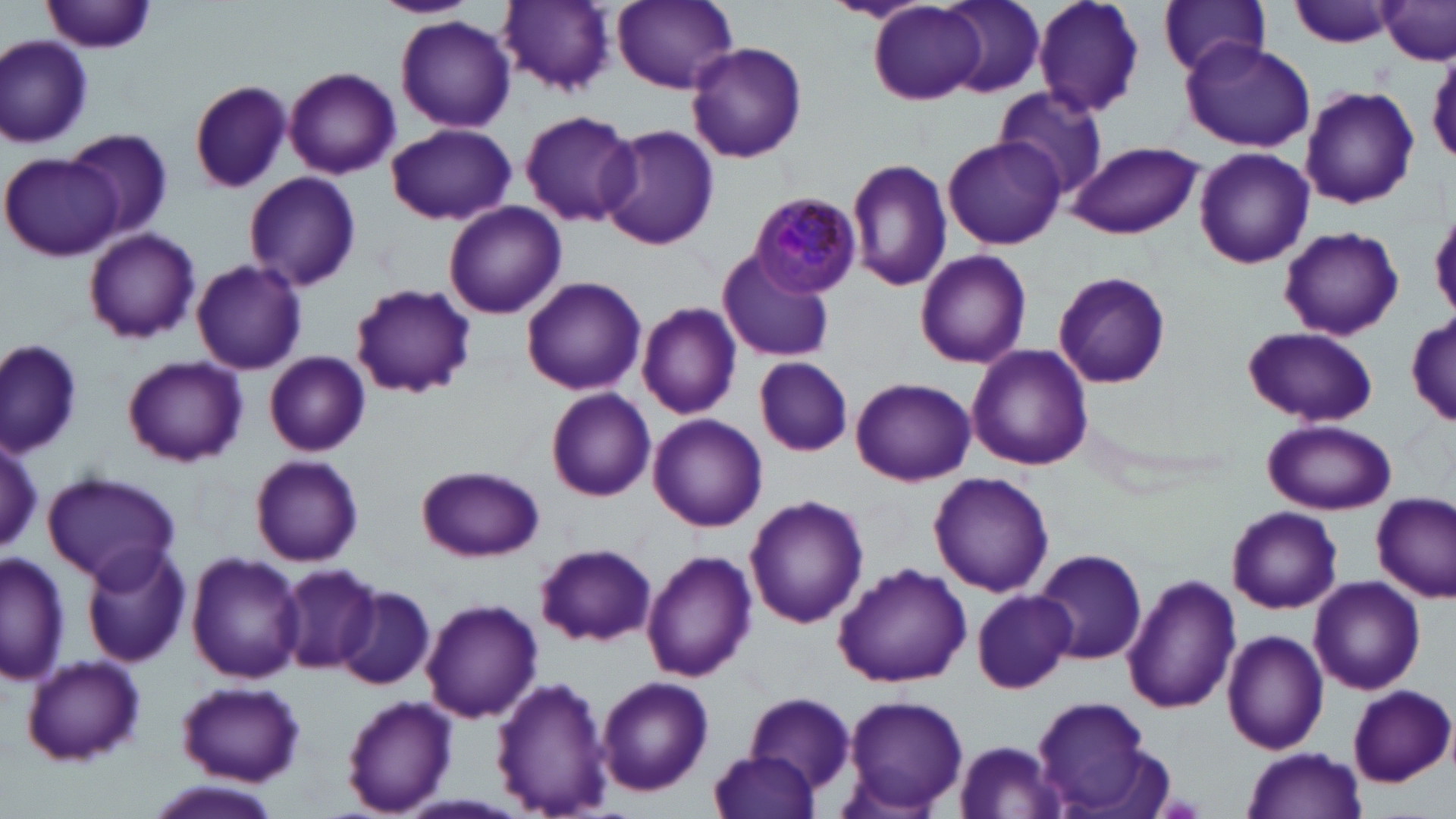

Approximate bounding boxes as [x1, y1, x2, y2] in pixels. Uninfected red blood cell locations: [374, 0, 476, 18], [497, 0, 615, 94], [612, 0, 739, 92], [824, 0, 933, 25], [941, 0, 1045, 97], [1031, 0, 1145, 120], [1158, 0, 1270, 78], [1287, 0, 1399, 49], [43, 1, 156, 55], [1379, 1, 1455, 64], [869, 2, 987, 104], [395, 15, 517, 133], [0, 34, 95, 148], [1179, 39, 1316, 152], [686, 41, 808, 165], [284, 66, 401, 179], [190, 80, 292, 193], [992, 85, 1108, 200], [1300, 86, 1420, 209], [519, 108, 639, 228], [387, 124, 515, 225], [597, 125, 720, 251], [67, 127, 172, 240], [943, 138, 1065, 250], [1066, 141, 1202, 240], [1193, 147, 1315, 269], [2, 151, 126, 259], [847, 158, 952, 292], [243, 170, 362, 291], [442, 200, 567, 320], [1278, 226, 1405, 342], [83, 227, 200, 343], [717, 247, 835, 362], [915, 249, 1033, 369], [191, 259, 306, 375], [1052, 270, 1171, 390], [520, 278, 647, 397], [350, 284, 477, 399], [637, 300, 743, 420], [1408, 314, 1455, 428], [1242, 326, 1381, 429], [1, 337, 85, 458], [966, 344, 1094, 471], [264, 352, 370, 456], [122, 355, 247, 466], [754, 357, 854, 456], [851, 377, 976, 487], [546, 389, 656, 504], [647, 413, 767, 531], [1264, 419, 1397, 514], [2, 430, 43, 558], [250, 455, 364, 566], [416, 464, 544, 562], [43, 470, 183, 587], [930, 470, 1055, 596], [1372, 493, 1455, 600], [745, 494, 869, 629], [1226, 505, 1343, 615], [79, 542, 192, 667], [535, 543, 658, 647], [1031, 546, 1149, 665], [642, 549, 757, 683], [2, 552, 69, 687], [187, 553, 303, 683], [832, 562, 973, 687], [275, 566, 379, 673], [1122, 574, 1241, 715], [1308, 575, 1428, 694], [335, 586, 434, 689], [971, 588, 1076, 692], [422, 597, 542, 722], [1223, 630, 1329, 755], [20, 654, 145, 766], [491, 675, 615, 817], [595, 676, 715, 796], [177, 682, 305, 786], [1347, 686, 1454, 787], [741, 692, 856, 802], [839, 694, 968, 815], [341, 695, 459, 817], [1030, 695, 1167, 817], [950, 740, 1072, 817], [1242, 746, 1367, 819], [709, 751, 820, 819], [144, 783, 286, 819]. Plasmodium malariae-infected red blood cell locations: [749, 192, 863, 298]. Slide-level diagnosis: Plasmodium malariae. May-Grünwald-Giemsa-stained preparation. One field of a larger specimen. Image is 1456×819 pixels. 1000x magnification. Light microscopy. Thin blood smear.